Give the extent of all Plasmodium falciparum-infected red blood cells.
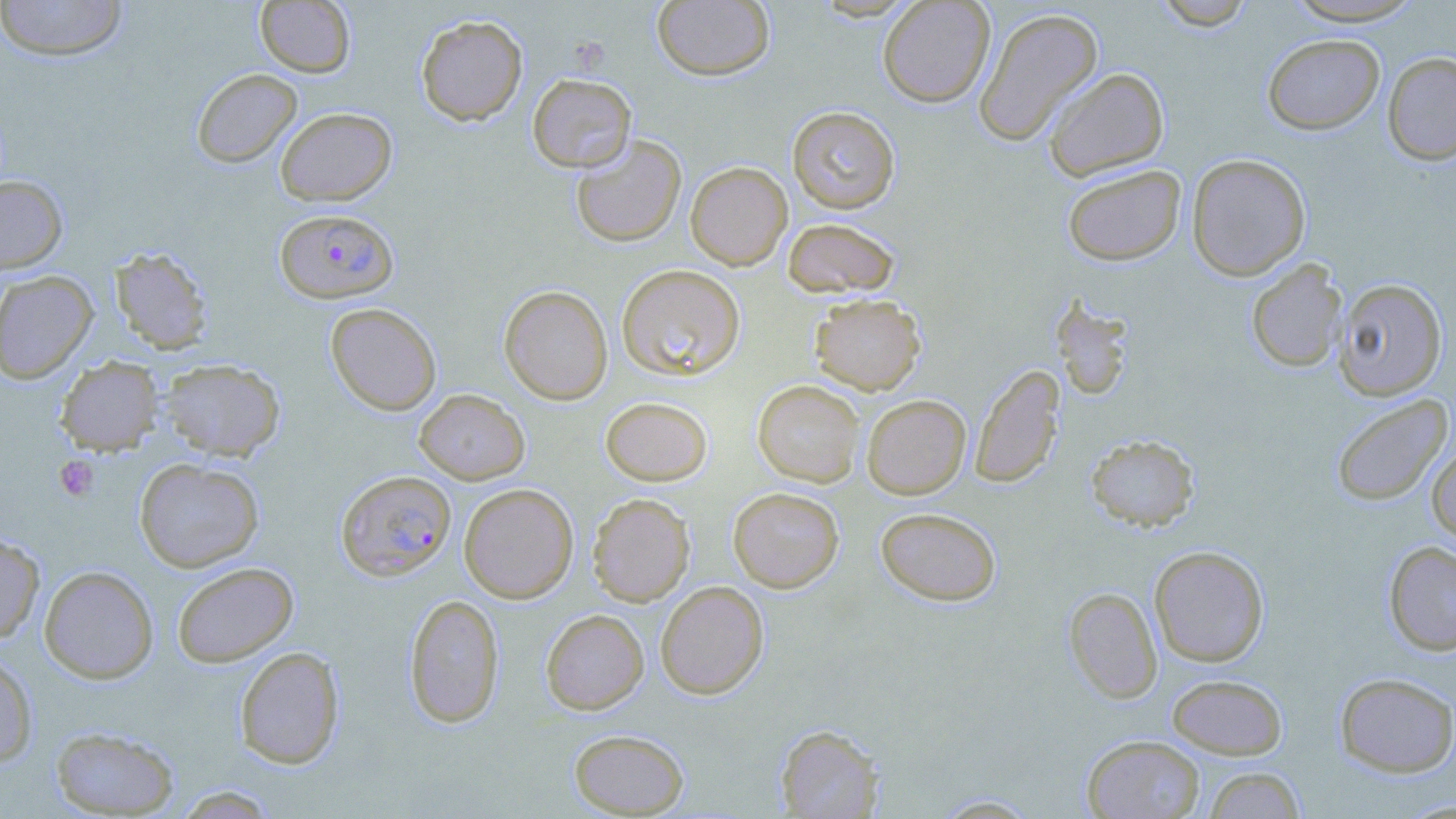
Approximate bounding boxes as (x1, y1, x2, y2) in pixels.
Plasmodium falciparum-infected red blood cells: (275, 208, 398, 304), (336, 470, 456, 581).

Uninfected red blood cell locations: (0, 0, 128, 61), (877, 0, 995, 107), (1152, 0, 1256, 30), (1282, 0, 1425, 26), (255, 1, 356, 77), (652, 1, 775, 81), (973, 7, 1103, 146), (416, 14, 528, 126), (1262, 33, 1385, 135), (1382, 52, 1456, 165), (1044, 67, 1169, 181), (191, 68, 302, 168), (527, 73, 637, 173), (787, 106, 900, 213), (275, 107, 397, 206), (570, 134, 686, 248), (1186, 153, 1311, 281), (685, 161, 792, 270), (1062, 164, 1186, 266), (0, 176, 68, 272), (782, 218, 900, 299), (109, 247, 214, 355), (1245, 260, 1348, 373), (617, 264, 746, 381), (0, 270, 98, 384), (1334, 278, 1448, 400), (499, 285, 613, 405), (809, 293, 926, 395), (1049, 296, 1136, 402), (325, 303, 442, 415), (54, 356, 163, 456), (159, 359, 285, 462), (970, 364, 1065, 489), (752, 380, 864, 487), (413, 389, 530, 484), (861, 394, 971, 499), (1331, 394, 1453, 507), (600, 397, 713, 486), (1085, 433, 1200, 532), (1427, 445, 1456, 545), (134, 458, 264, 572), (459, 483, 578, 603), (728, 487, 844, 592), (587, 493, 695, 606), (875, 507, 1002, 606), (0, 531, 45, 643), (1383, 541, 1456, 655), (1149, 545, 1269, 667), (172, 561, 299, 667), (39, 565, 158, 684), (655, 581, 769, 699), (1064, 587, 1162, 703), (403, 593, 504, 728), (540, 609, 649, 714), (234, 646, 344, 770), (0, 652, 38, 768), (1334, 672, 1456, 777), (1167, 674, 1287, 759), (775, 724, 884, 817), (50, 726, 179, 817), (568, 728, 689, 817), (1082, 734, 1205, 819), (1202, 766, 1305, 818), (172, 786, 280, 818), (930, 793, 1043, 817). Platelet locations: (54, 455, 100, 501). Slide-level diagnosis: Plasmodium falciparum. Image is 1456×819 pixels. May-Grünwald-Giemsa-stained preparation. One field of a larger specimen. 1000x magnification. Optical microscopy. Thin blood smear.